Outline each blood parasite and name the species.
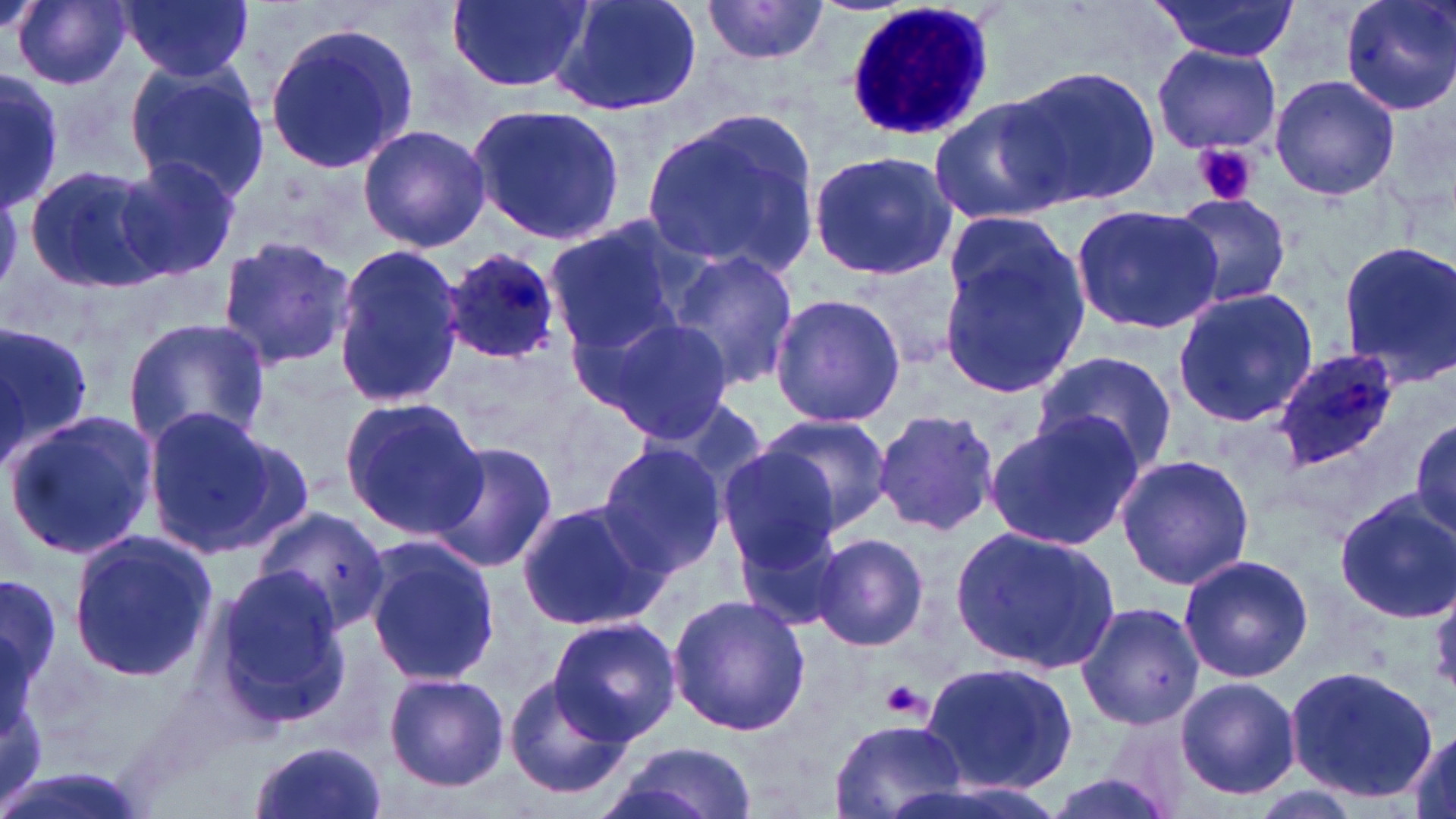
Approximate bounding boxes as (x1,y1)-(x2,y2) corner pairs in pixels.
Plasmodium ovale-infected red blood cells: (443,249)-(563,363), (1272,349)-(1402,471).
No Plasmodium falciparum, Plasmodium malariae, Plasmodium vivax, Babesia divergens, or Trypanosoma brucei observed.

slide-level diagnosis = Plasmodium ovale
uninfected red blood cell locations = approximate bounding boxes as (x1,y1)-(x2,y2) corner pairs in pixels: (13,0)-(133,90), (120,0)-(254,82), (447,0)-(592,92), (544,0)-(702,117), (1148,0)-(1300,62), (1338,0)-(1456,115), (700,1)-(831,65), (262,17)-(423,174), (1152,43)-(1281,155), (122,59)-(267,201), (1008,65)-(1160,211), (0,69)-(65,212), (1269,75)-(1400,203), (930,95)-(1070,223), (465,102)-(627,246), (640,106)-(822,282), (357,124)-(491,252), (806,151)-(959,282), (113,157)-(240,280), (24,164)-(171,290), (1168,192)-(1293,309), (1069,202)-(1222,335), (942,212)-(1072,316), (541,218)-(691,353), (214,234)-(358,371), (936,234)-(1091,401), (1337,239)-(1456,383), (330,243)-(467,406), (666,248)-(800,394), (847,258)-(963,371), (1171,286)-(1318,428), (767,293)-(907,429), (577,312)-(730,443), (123,317)-(271,451), (0,320)-(97,465), (1030,351)-(1176,476), (339,397)-(486,541), (142,408)-(304,554), (871,408)-(1000,540), (4,409)-(160,563), (986,411)-(1143,550), (758,415)-(893,533), (1411,417)-(1455,538), (426,440)-(556,575), (596,442)-(729,576), (716,447)-(842,571), (1115,454)-(1255,591), (1334,490)-(1456,622), (516,498)-(667,633), (256,505)-(388,635), (729,522)-(849,637), (951,526)-(1117,672), (68,530)-(216,682), (809,533)-(932,652), (362,538)-(500,686), (1177,554)-(1314,683), (211,568)-(348,727), (0,569)-(64,706), (667,594)-(810,737), (1075,602)-(1204,731), (549,616)-(682,742), (920,660)-(1079,794), (1285,663)-(1438,800), (383,671)-(510,791), (504,671)-(633,798), (1172,676)-(1304,800), (829,716)-(968,819), (1404,727)-(1456,819), (248,740)-(387,819), (607,743)-(756,819)
field of view = one of a larger specimen
preparation = thin blood film
stain = May-Grünwald-Giemsa
modality = light microscopy
magnification = 1000x
image size = 1456×819 pixels
white blood cell locations = approximate bounding boxes as (x1,y1)-(x2,y2) corner pairs in pixels: (842,3)-(992,144)
platelet locations = approximate bounding boxes as (x1,y1)-(x2,y2) corner pairs in pixels: (1193,142)-(1260,207), (882,680)-(928,720)